Give the position of every leukocyte visible.
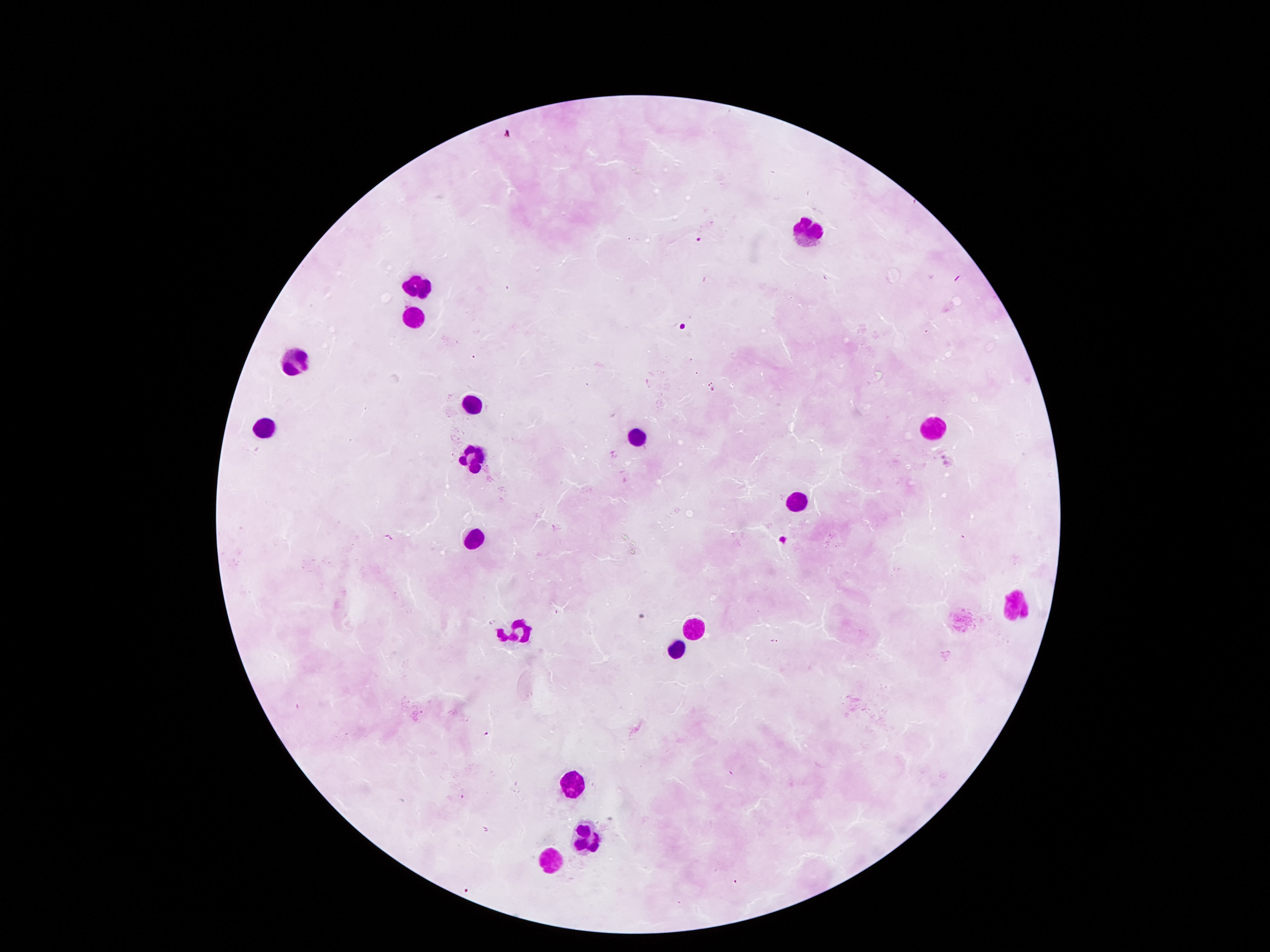

Approximate centers as {x, y} in pixels.
Leukocytes: {807, 227}, {421, 281}, {411, 317}, {293, 359}, {474, 398}, {266, 430}, {931, 431}, {634, 438}, {473, 460}, {799, 499}, {474, 538}, {1015, 600}, {697, 626}, {510, 634}, {678, 648}, {573, 781}, {586, 835}, {550, 856}.

capture: smartphone camera through the microscope eyepiece
field_of_view: single
image_size: 1270×952 pixels
stain: Giemsa
magnification: 100x
patient_malaria_status: uninfected
preparation: thick blood smear